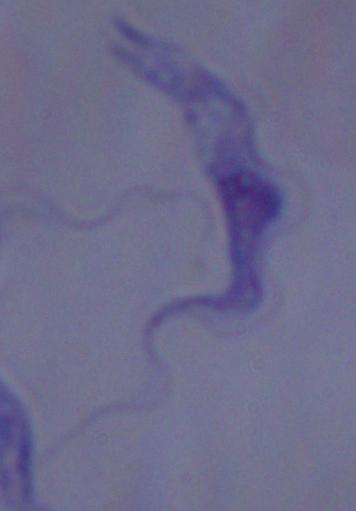
Summary:
  - Modality: micrograph
  - Identification: trypanosome
  - Magnification: 1000x